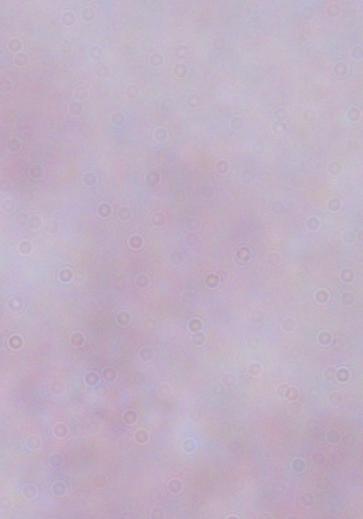
Captured at 1000x magnification. Micrograph. A trypanosome is shown.